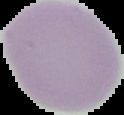

Summary:
  - Malaria status: uninfected
  - Image type: segmented cell region with the area outside set to black
  - Image size: 124×115 pixels
  - Preparation: thin blood film